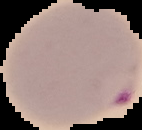 Result: Plasmodium parasites detected. Image is 142×130 pixels. From a thin blood smear. The area outside the segmented cell region is set to black.